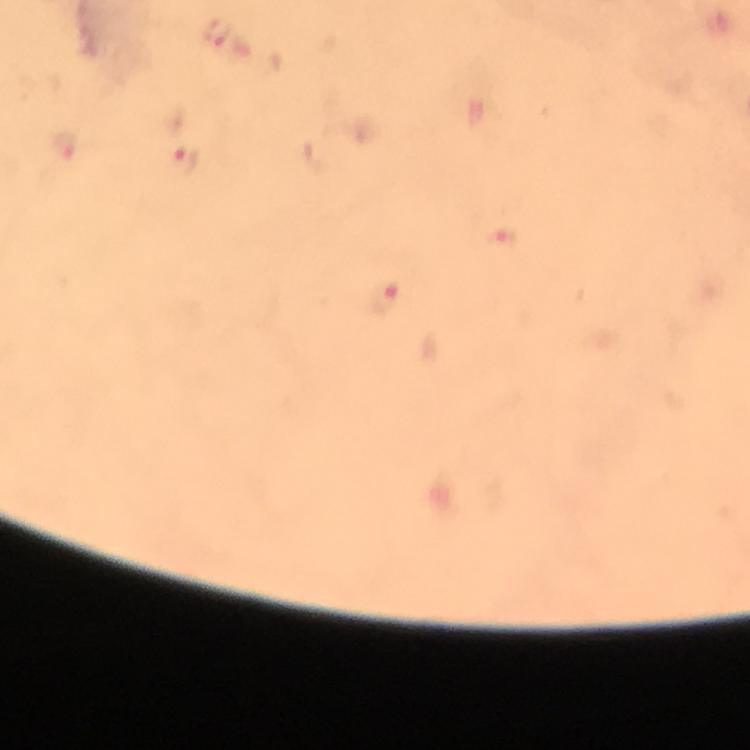
{
  "capture": "smartphone camera through the microscope",
  "cropped_from": "one field of view",
  "immersion_oil": "applied",
  "magnification": "100x",
  "context": "from a malaria diagnostic workup",
  "malaria_parasite_locations": "approximate centers as {x, y} in pixels: {216, 32}, {182, 162}, {384, 299}",
  "preparation": "thick smear",
  "stain": "Giemsa",
  "image_size": "750×750 pixels"
}